Name the parasite shown.
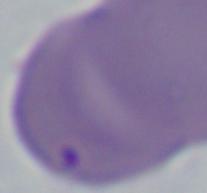
This is Babesia.

Summary:
  - Magnification: 1000x
  - Modality: micrograph